Assess the morphology of the erythrocytes.
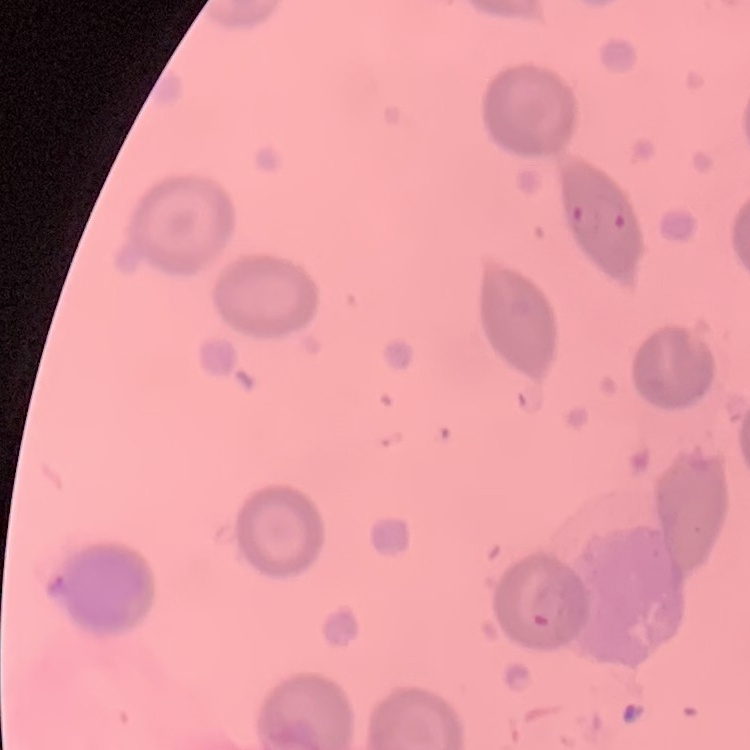
They show no rouleaux formation.

Summary:
  - Stain: Field's or Giemsa
  - Image type: one tile cut from a larger photomicrograph
  - Preparation: thin blood film